Report the malaria status of this cell.
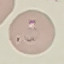

Parasitized.

image type = automatically extracted cell patch, resized to 64 × 64 pixels
capture = smartphone camera at the microscope eyepiece
preparation = thin blood smear
stain = Giemsa